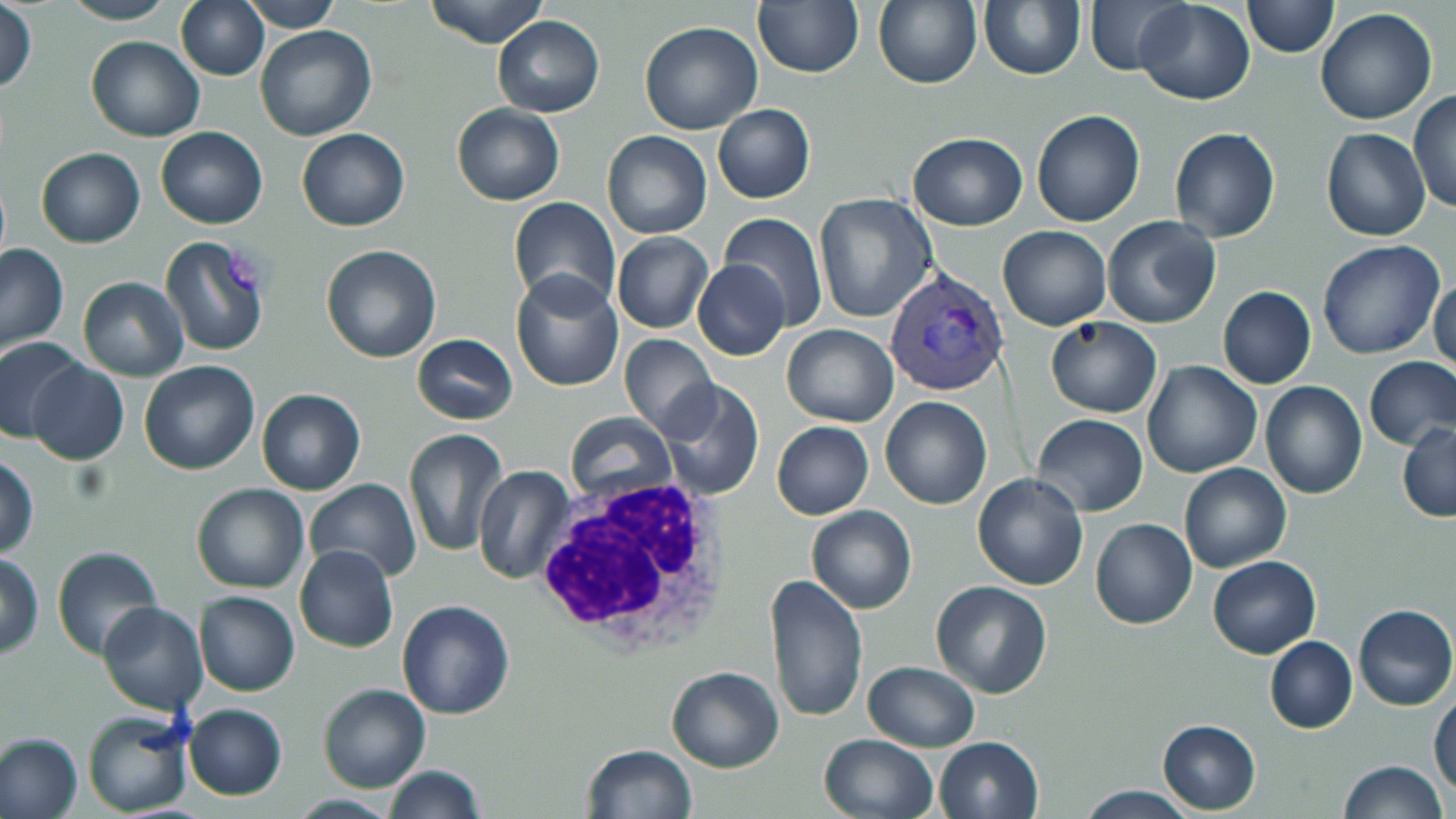
slide-level diagnosis = Plasmodium vivax
white blood cell locations = approximate bounding boxes as (x1,y1)-(x2,y2) corner pairs in pixels: (530,472)-(741,659)
Plasmodium vivax-infected red blood cell locations = approximate bounding boxes as (x1,y1)-(x2,y2) corner pairs in pixels: (883,265)-(1009,398)
uninfected red blood cell locations = approximate bounding boxes as (x1,y1)-(x2,y2) corner pairs in pixels: (62,0)-(177,26), (174,0)-(269,80), (240,0)-(342,30), (425,0)-(547,48), (1082,0)-(1190,78), (1133,0)-(1256,104), (1242,0)-(1338,57), (752,1)-(864,78), (873,1)-(982,88), (979,2)-(1084,80), (1,3)-(38,95), (1315,8)-(1438,125), (493,14)-(604,117), (639,20)-(764,134), (255,25)-(377,143), (85,35)-(205,141), (1408,90)-(1456,215), (452,104)-(565,204), (713,104)-(815,203), (1032,110)-(1145,227), (157,127)-(268,229), (1169,128)-(1281,244), (296,129)-(409,231), (1321,129)-(1431,242), (602,130)-(712,240), (907,133)-(1029,231), (36,147)-(145,248), (814,193)-(939,324), (508,198)-(621,313), (718,213)-(830,331), (1100,214)-(1222,330), (997,225)-(1111,329), (612,232)-(713,332), (159,235)-(270,356), (1317,238)-(1445,361), (0,242)-(70,354), (321,244)-(441,363), (693,258)-(790,360), (511,270)-(624,393), (1429,274)-(1456,377), (78,276)-(187,382), (1218,286)-(1317,389), (1045,317)-(1161,418), (782,323)-(898,428), (620,332)-(717,436), (411,333)-(518,424), (0,335)-(84,442), (1364,357)-(1456,449), (27,360)-(129,466), (139,361)-(261,475), (1142,361)-(1262,478), (658,379)-(765,499), (1260,381)-(1369,500), (256,388)-(365,495), (880,395)-(993,510), (1033,413)-(1147,516), (566,415)-(676,505), (772,421)-(873,519), (1398,422)-(1456,522), (403,428)-(510,559), (0,453)-(38,558), (1178,462)-(1292,572), (474,466)-(574,584), (972,473)-(1089,590), (301,480)-(421,585), (192,484)-(309,594), (807,504)-(917,615), (1090,518)-(1197,629), (293,545)-(400,652), (52,546)-(162,662), (1,553)-(44,657), (1207,555)-(1321,659), (765,573)-(869,723), (930,580)-(1052,698), (193,591)-(300,697), (396,600)-(515,720), (97,603)-(209,715), (1353,604)-(1456,712), (1265,636)-(1357,733), (862,661)-(980,752), (665,666)-(784,771), (318,683)-(431,793), (1431,693)-(1456,798), (182,704)-(287,800), (82,707)-(194,817), (1157,720)-(1261,813), (0,733)-(83,819), (818,733)-(939,819), (934,736)-(1044,819), (581,744)-(697,819), (1338,760)-(1447,819), (384,765)-(486,819), (1078,786)-(1195,818)
magnification = 1000x
image size = 1456×819 pixels
stain = May-Grünwald-Giemsa
preparation = thin blood film
modality = light microscopy
field of view = single